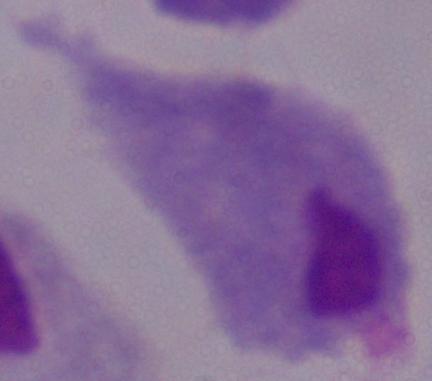

identification: trichomonad
magnification: 1000x
modality: photomicrograph